Locate platelets.
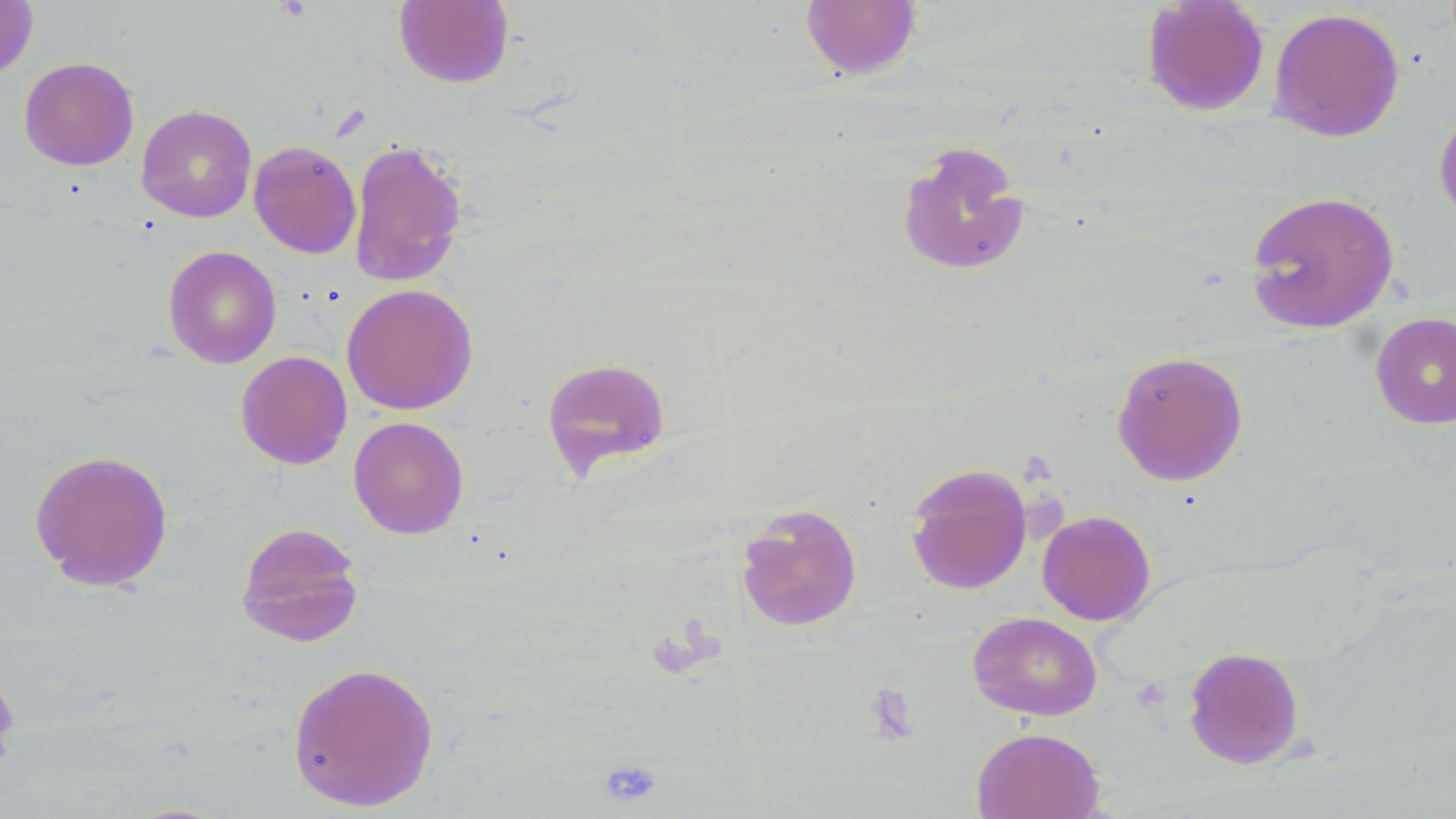

Approximate bounding boxes as (x1, y1, x2, y2) in pixels.
Platelets: (863, 684, 918, 742), (597, 758, 663, 809).

Summary:
  - Uninfected red blood cell locations: (394, 0, 514, 88), (1141, 0, 1270, 116), (0, 1, 38, 82), (800, 1, 922, 80), (1268, 7, 1405, 143), (18, 56, 139, 171), (135, 104, 257, 223), (1433, 105, 1456, 228), (348, 138, 468, 288), (248, 140, 361, 259), (895, 140, 1031, 278), (1244, 190, 1400, 334), (163, 245, 282, 369), (341, 283, 478, 415), (1370, 311, 1456, 429), (1111, 350, 1249, 486), (235, 351, 352, 470), (541, 357, 672, 480), (348, 416, 469, 539), (29, 448, 174, 592), (905, 463, 1033, 595), (735, 503, 862, 632), (1037, 509, 1156, 625), (235, 521, 365, 646), (968, 611, 1103, 721), (1183, 646, 1305, 769), (0, 661, 20, 781), (287, 661, 439, 812), (971, 727, 1105, 819)
  - Slide-level diagnosis: no evidence of blood parasites
  - Stain: May-Grünwald-Giemsa
  - Image size: 1456×819 pixels
  - Magnification: 1000x
  - Modality: light microscopy
  - Field of view: one of a larger specimen
  - Preparation: thin blood film